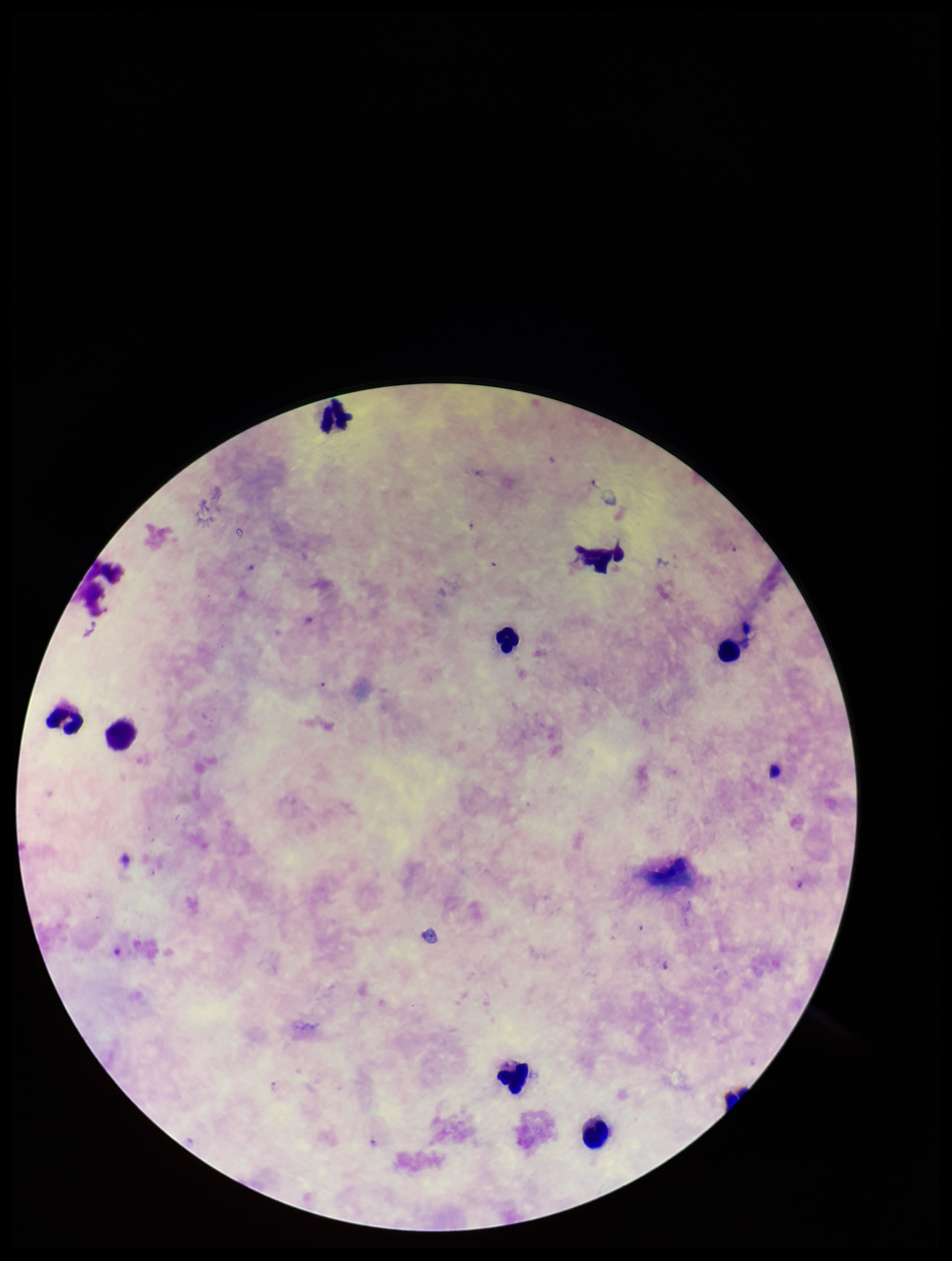

Summary:
  - Leukocyte count: 8
  - Field of view: single
  - Image size: 952×1261 pixels
  - Stain: Giemsa
  - Species reported for this patient: Plasmodium falciparum
  - Parasite count: 0
  - Preparation: thick smear
  - Capture: smartphone photograph through the microscope eyepiece
  - Plasmodium parasites: none identified
  - Patient malaria status: infected